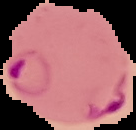

image type = segmented cell region with the area outside set to black
preparation = thin blood smear
result = Plasmodium parasites identified
image size = 136×130 pixels